Report the malaria status of this cell.
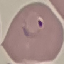

Parasitized.

Summary:
  - Stain: Giemsa
  - Preparation: thin smear
  - Capture: smartphone camera at the microscope eyepiece
  - Image type: cell patch, automatically extracted from a larger field of view and resized to 64 × 64 pixels